Locate every Trypanosoma brucei.
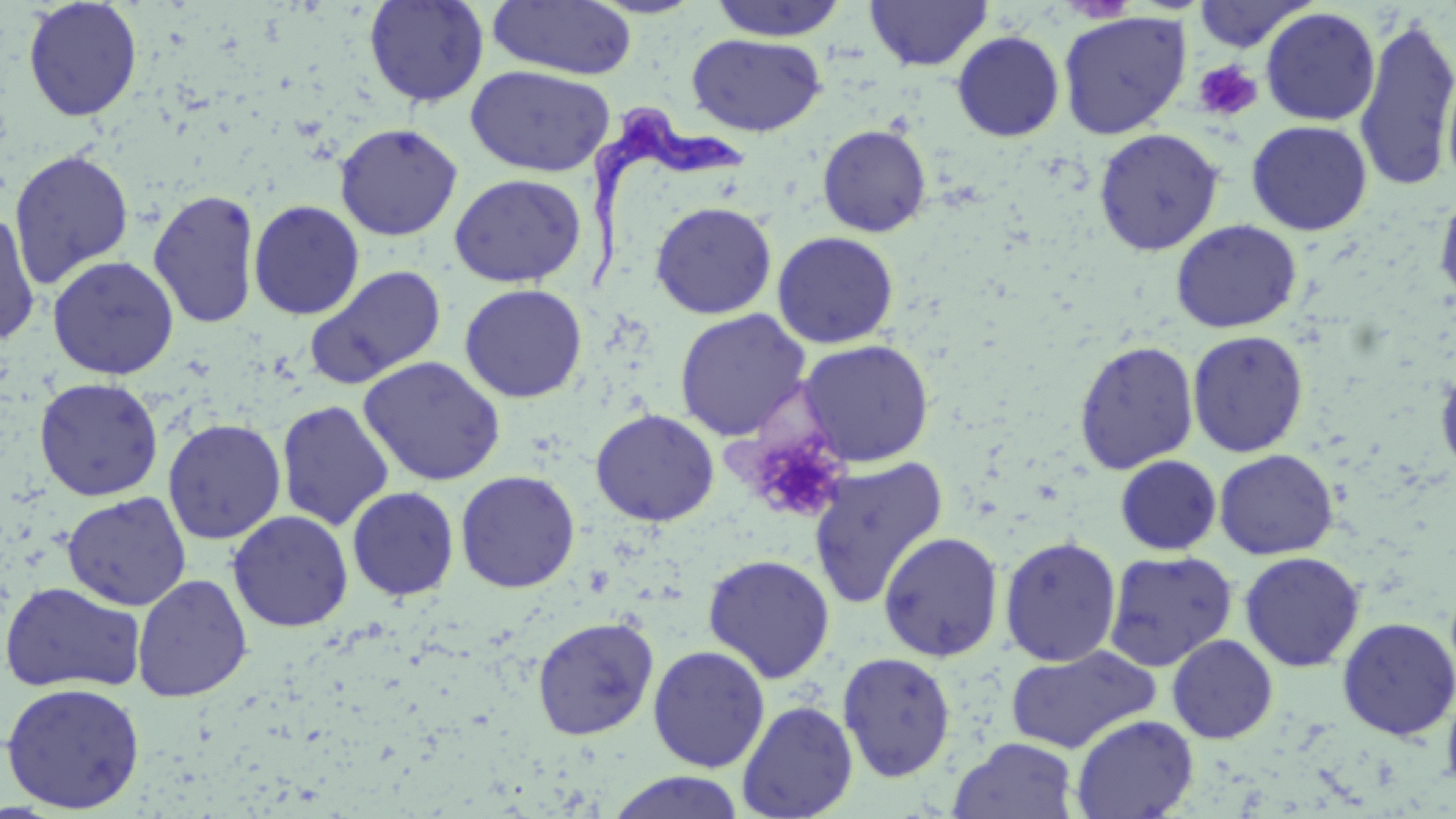

Approximate bounding boxes as (x1,y1)-(x2,y2) corner pairs in pixels.
Trypanosoma brucei: (584,103)-(747,299).

Uninfected red blood cell locations: (22,0)-(142,122), (363,0)-(489,108), (585,0)-(707,18), (708,0)-(848,41), (865,0)-(992,72), (488,1)-(637,80), (1191,1)-(1315,53), (1261,6)-(1381,126), (1057,11)-(1191,139), (1353,13)-(1456,195), (951,31)-(1065,141), (687,33)-(826,137), (465,65)-(615,177), (1246,120)-(1372,236), (334,122)-(463,241), (817,124)-(932,237), (1093,128)-(1224,256), (9,149)-(134,288), (449,174)-(587,287), (1433,185)-(1456,310), (147,189)-(261,329), (247,199)-(365,320), (649,201)-(777,319), (0,210)-(41,347), (1170,219)-(1302,334), (772,231)-(899,349), (47,255)-(179,380), (304,265)-(447,390), (459,283)-(588,403), (674,309)-(812,442), (1187,330)-(1309,457), (797,339)-(935,467), (1073,340)-(1199,474), (359,356)-(506,486), (1435,362)-(1456,482), (33,376)-(163,501), (276,400)-(395,531), (591,409)-(720,526), (162,418)-(286,544), (1214,449)-(1339,560), (1115,455)-(1222,556), (808,456)-(949,610), (455,470)-(580,593), (347,486)-(460,601), (62,491)-(192,611), (228,510)-(353,632), (878,531)-(1004,662), (999,536)-(1122,668), (1104,550)-(1238,671), (1239,551)-(1365,672), (702,553)-(836,683), (132,574)-(253,702), (0,581)-(147,695), (532,615)-(659,740), (1336,616)-(1456,740), (1166,634)-(1279,744), (1004,644)-(1162,754), (648,645)-(770,773), (837,651)-(956,782), (1,681)-(145,814), (1441,684)-(1456,799), (737,700)-(859,818), (1070,714)-(1199,819), (949,736)-(1079,819), (605,771)-(747,819). Platelet locations: (1192,59)-(1263,122), (746,432)-(848,523). Slide-level diagnosis: Trypanosoma brucei. Optical microscopy. May-Grünwald-Giemsa stain. Captured at 1000x magnification. Image is 1456×819 pixels. One field of a larger specimen. Thin blood smear.